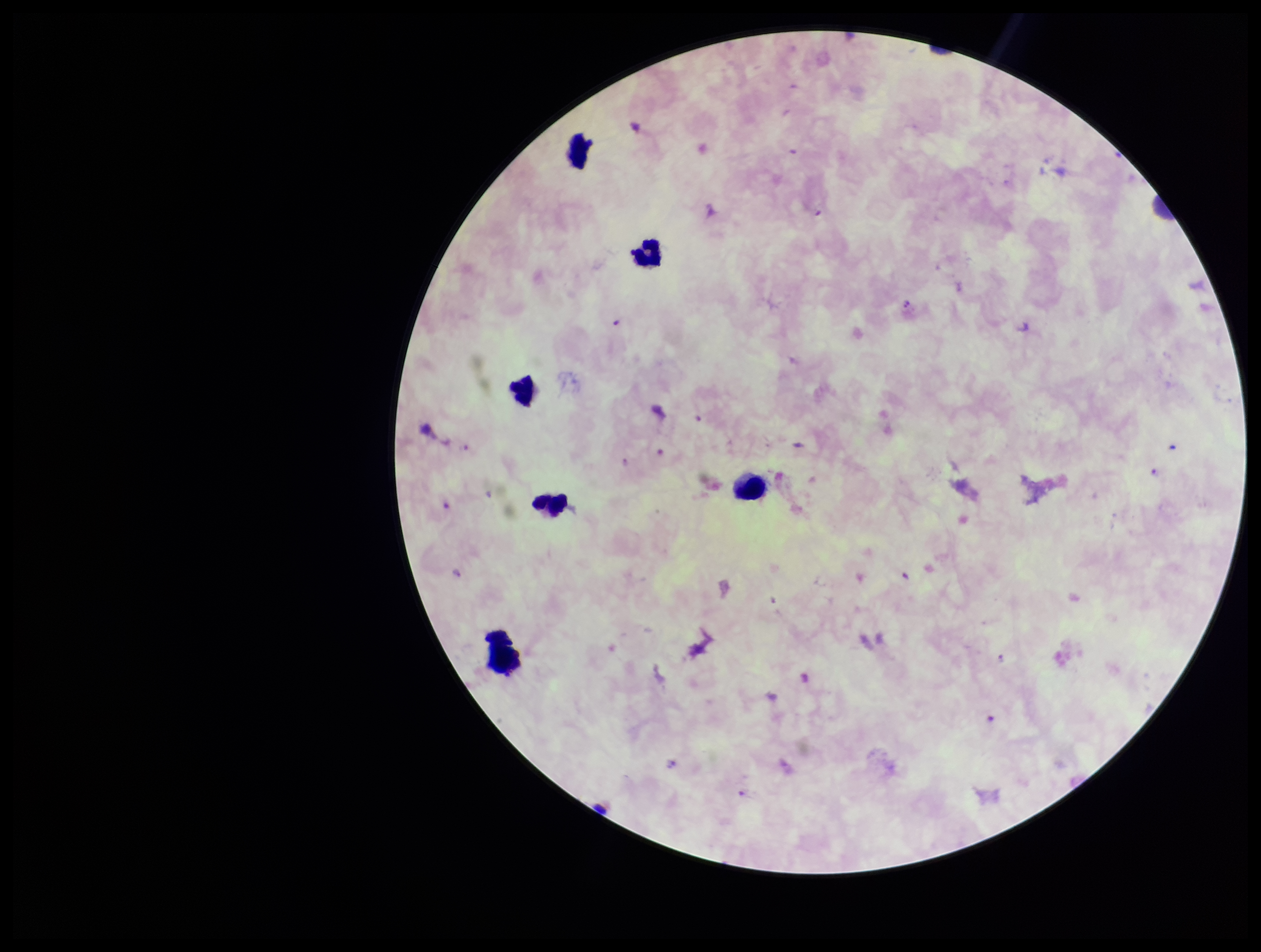
Summary:
  - Preparation: thick blood smear
  - Plasmodium parasites: detected
  - Stain: Giemsa
  - Field of view: single
  - Parasite count: 8
  - Image size: 1261×952 pixels
  - Capture: smartphone photograph through the microscope eyepiece
  - Leukocyte count: 6
  - Species reported for this patient: Plasmodium falciparum
  - Patient malaria status: positive